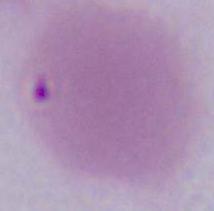

Micrograph. A red blood cell is shown. 1000x magnification.